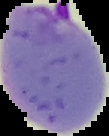

{
  "image_size": "109×136 pixels",
  "image_type": "segmented cell region with the area outside set to black",
  "malaria_status": "parasitized",
  "preparation": "thin blood smear"
}